Name the cell type shown.
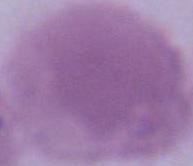
This is an erythrocyte.

Summary:
  - Magnification: 1000x
  - Modality: micrograph